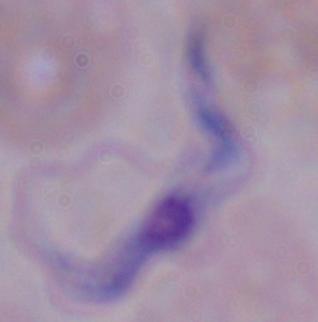

magnification = 1000x
identification = trypanosome
modality = micrograph